Name the parasite shown.
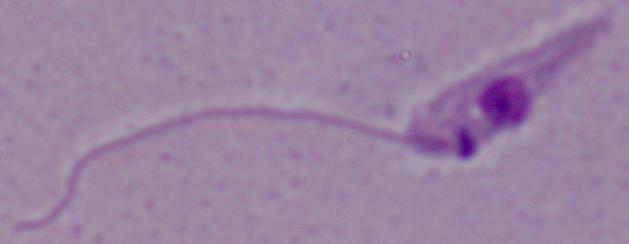
Leishmania.

magnification: 1000x
modality: micrograph